Report the malaria status.
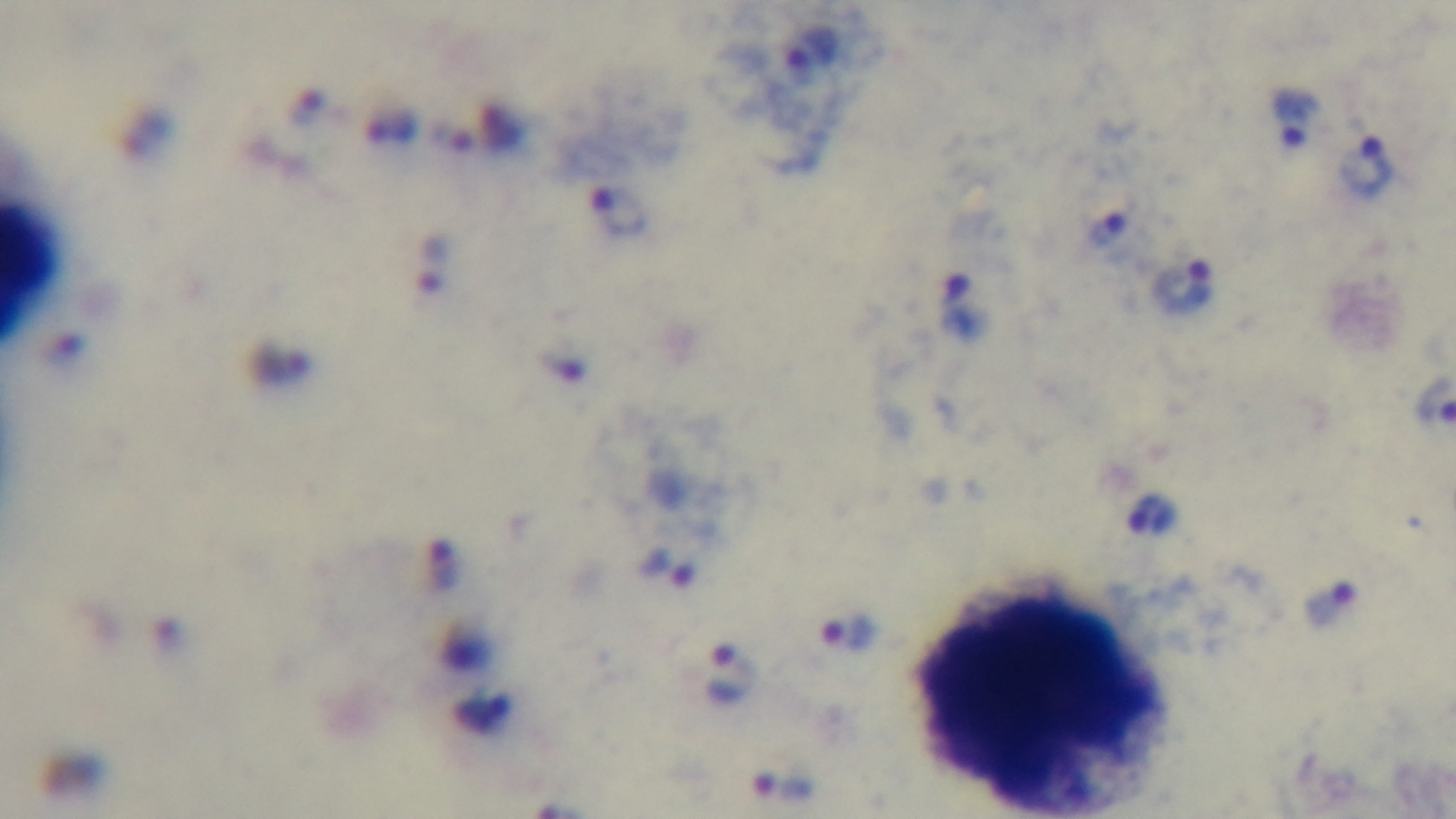

Positive.

Summary:
  - Capture: mounted 4K digital camera
  - Modality: light microscopy
  - Stain: Giemsa
  - Preparation: thick smear
  - Objective: 100x oil immersion
  - Field of view: one from the slide